Report the malaria status of this cell.
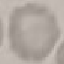
It is uninfected.

Summary:
  - Preparation: thin smear
  - Image type: cell patch, automatically extracted from a larger field of view and resized to 64 × 64 pixels
  - Capture: smartphone camera at the microscope eyepiece
  - Stain: Giemsa